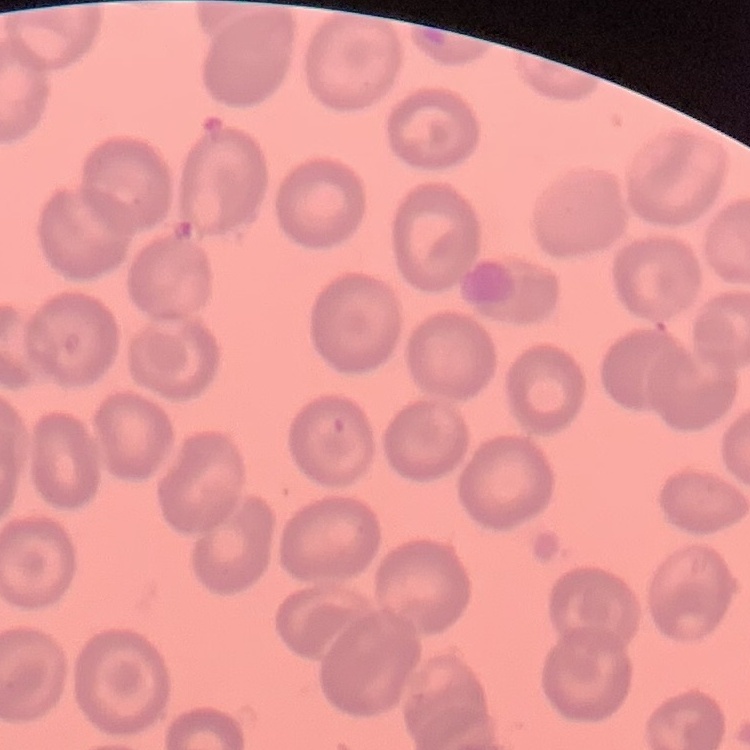

red blood cell morphology = no rouleaux formation
image type = one tile cut from a larger photomicrograph
preparation = thin peripheral smear
stain = Field's or Giemsa